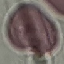

result = no malaria parasites seen
image type = cell patch, automatically extracted from a larger field of view and resized to 64 × 64 pixels
capture = smartphone through the microscope eyepiece
preparation = thin blood smear
stain = Giemsa